Name the parasite shown.
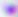

Toxoplasma gondii.

Captured at 400x magnification. Micrograph.